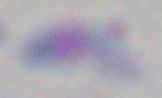

Micrograph. 1000x magnification. Toxoplasma gondii is seen.